Identify the parasite.
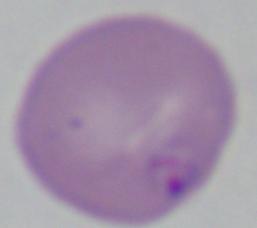

Babesia.

Micrograph. 1000x magnification.